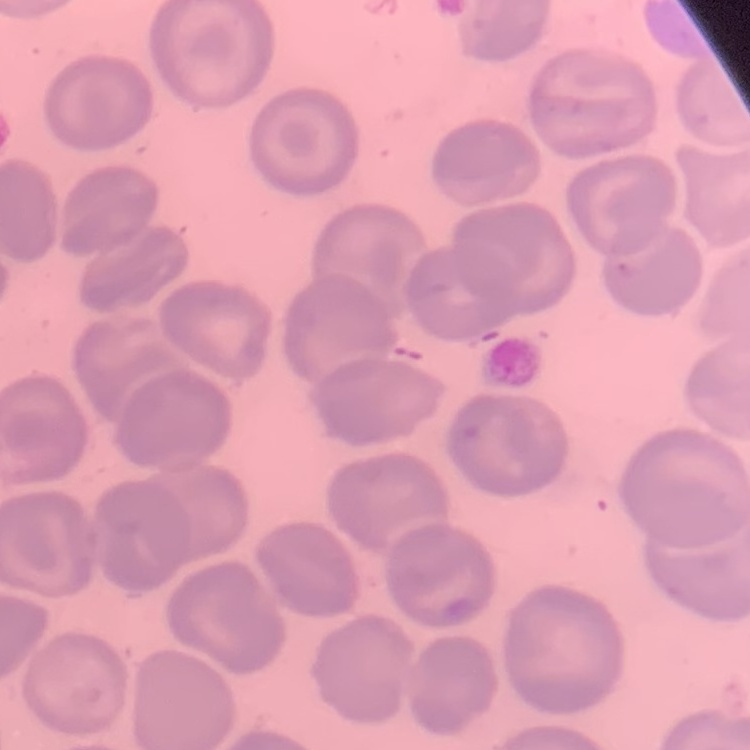
erythrocyte_morphology: no rouleaux formation
preparation: thin blood smear
stain: Field's or Giemsa
image_type: one tile cut from a larger photomicrograph